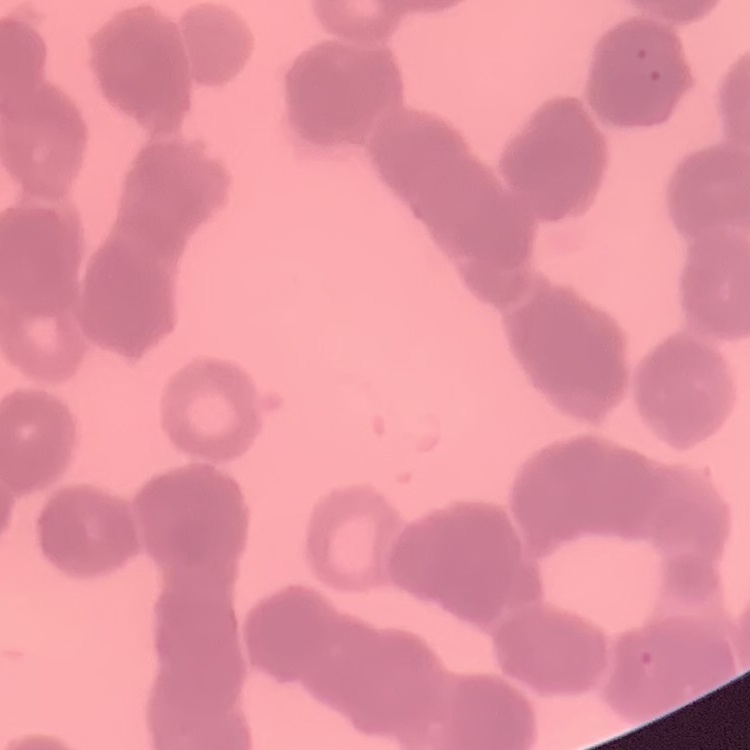
The erythrocytes show rouleaux formation. Square crop of a larger photomicrograph. Thin blood smear. Field's or Giemsa stain.